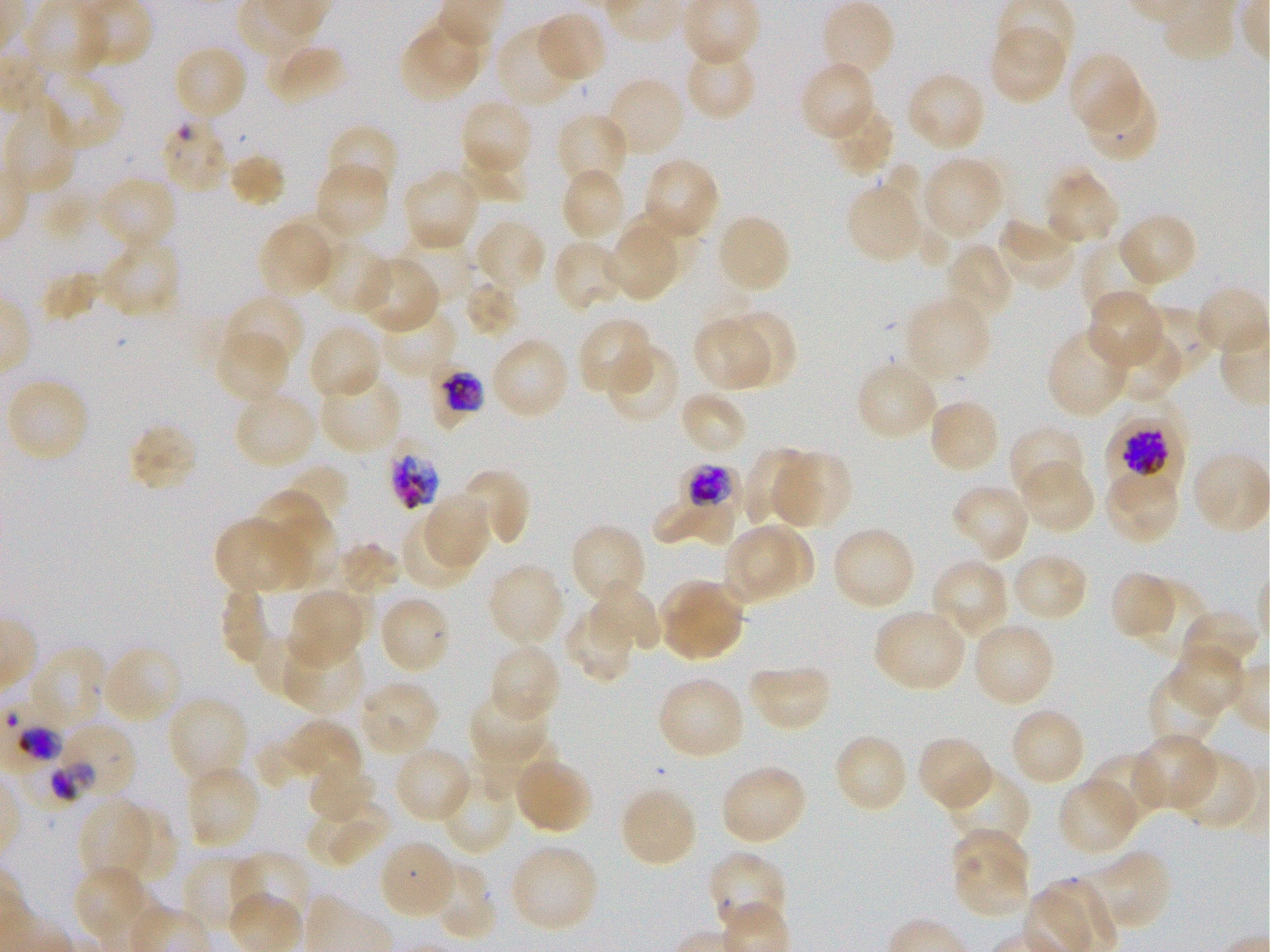

Approximate bounding boxes as [x1, y1, x2, y2] in pixels. Not every red blood cell is marked. A life-cycle stage — or a range of stages, where the recorded stages span more than one — follows each staged infected red blood cell.
Summary:
  - Locations of uninfected red blood cells: [820, 0, 896, 82], [535, 10, 608, 85], [400, 14, 489, 101], [494, 23, 582, 110], [988, 24, 1067, 106], [171, 43, 248, 123], [265, 43, 347, 106], [683, 43, 757, 121], [1068, 51, 1145, 136], [799, 60, 877, 143], [36, 71, 123, 152], [905, 71, 987, 153], [602, 75, 686, 159], [1081, 79, 1160, 164], [458, 98, 535, 182], [827, 102, 896, 178], [3, 105, 80, 198], [555, 112, 629, 193], [324, 124, 399, 203], [460, 150, 528, 202], [228, 153, 285, 207], [920, 154, 1006, 244], [641, 157, 720, 242], [878, 159, 957, 274], [314, 161, 390, 241], [560, 165, 628, 244], [1043, 167, 1122, 248], [401, 168, 481, 253], [96, 175, 177, 252], [845, 175, 926, 265], [626, 208, 698, 276], [1115, 210, 1199, 288], [714, 212, 792, 295], [473, 217, 548, 295], [996, 217, 1079, 292], [258, 222, 331, 295], [607, 230, 678, 302], [1083, 232, 1163, 312], [397, 233, 473, 304], [95, 235, 179, 319], [316, 239, 391, 314], [551, 239, 630, 313], [946, 242, 1016, 322], [353, 256, 441, 334], [35, 260, 108, 332], [464, 280, 518, 338], [1194, 284, 1270, 357], [1085, 289, 1165, 370], [221, 294, 305, 375], [902, 294, 992, 384], [1141, 299, 1221, 380], [376, 305, 459, 381], [694, 314, 777, 392], [716, 315, 799, 394], [577, 316, 655, 398], [308, 322, 383, 402], [1046, 325, 1133, 419], [1110, 325, 1185, 405], [215, 328, 291, 404], [489, 335, 571, 422], [603, 343, 681, 426], [855, 359, 939, 442], [318, 370, 403, 455], [5, 378, 92, 464], [233, 390, 318, 470], [678, 391, 749, 456], [927, 398, 1001, 475], [128, 422, 198, 493], [1009, 424, 1087, 505], [741, 446, 814, 525], [768, 450, 853, 530], [1191, 452, 1270, 535], [1018, 459, 1096, 535], [1103, 463, 1181, 544], [280, 464, 348, 533], [456, 468, 531, 547], [950, 483, 1031, 564], [253, 490, 336, 587], [650, 491, 739, 551], [422, 493, 490, 571], [399, 513, 477, 592], [214, 516, 308, 596], [721, 522, 814, 605], [570, 523, 648, 609], [830, 525, 917, 612], [334, 541, 399, 596], [1008, 551, 1089, 624], [930, 557, 1011, 641], [486, 563, 565, 649], [1108, 571, 1179, 642], [1129, 577, 1207, 665], [659, 578, 746, 663], [586, 582, 661, 655], [222, 586, 271, 664], [286, 588, 370, 667], [377, 594, 451, 675], [563, 603, 636, 684], [871, 608, 969, 693], [1178, 608, 1262, 679], [970, 620, 1056, 709], [254, 630, 322, 697], [284, 642, 366, 715], [488, 642, 561, 724], [100, 643, 186, 725], [28, 645, 108, 732], [1167, 647, 1246, 718], [746, 662, 832, 733], [1146, 668, 1226, 752], [656, 675, 746, 760], [357, 678, 440, 758], [469, 690, 550, 770], [166, 695, 250, 787], [1008, 705, 1087, 788], [266, 719, 362, 791], [833, 733, 910, 814], [1131, 733, 1219, 812], [916, 734, 995, 812], [477, 742, 551, 795], [393, 744, 473, 824], [1170, 748, 1259, 832], [1088, 752, 1167, 827], [513, 754, 593, 834], [307, 763, 376, 823], [719, 763, 807, 846], [184, 764, 262, 851], [942, 767, 1029, 846], [438, 769, 515, 856], [1057, 776, 1141, 857], [618, 785, 698, 869], [306, 790, 390, 868], [78, 798, 165, 888], [121, 807, 175, 883], [952, 826, 1033, 896], [378, 838, 458, 921], [508, 842, 599, 932], [949, 849, 1031, 919], [1076, 850, 1171, 934], [231, 851, 312, 936], [708, 851, 789, 937], [180, 853, 264, 937], [431, 859, 496, 942], [73, 864, 153, 944]
  - Locations of infected red blood cells: [426, 357, 488, 436] trophozoite; [1100, 414, 1185, 506] late trophozoite to late schizont; [671, 456, 749, 523] late trophozoite to early schizont
  - Locations of red blood cells of indeterminate infection status: [160, 117, 229, 195], [391, 449, 440, 510], [49, 722, 137, 804]
  - Field of view: single
  - Stain: Giemsa
  - Image size: 1270×952 pixels
  - Preparation: thin blood film
  - Donor blood group: O+
  - Culture: static in-vitro Plasmodium falciparum strain 3D7
  - Objective: 100x, oil immersion, numerical aperture 1.25